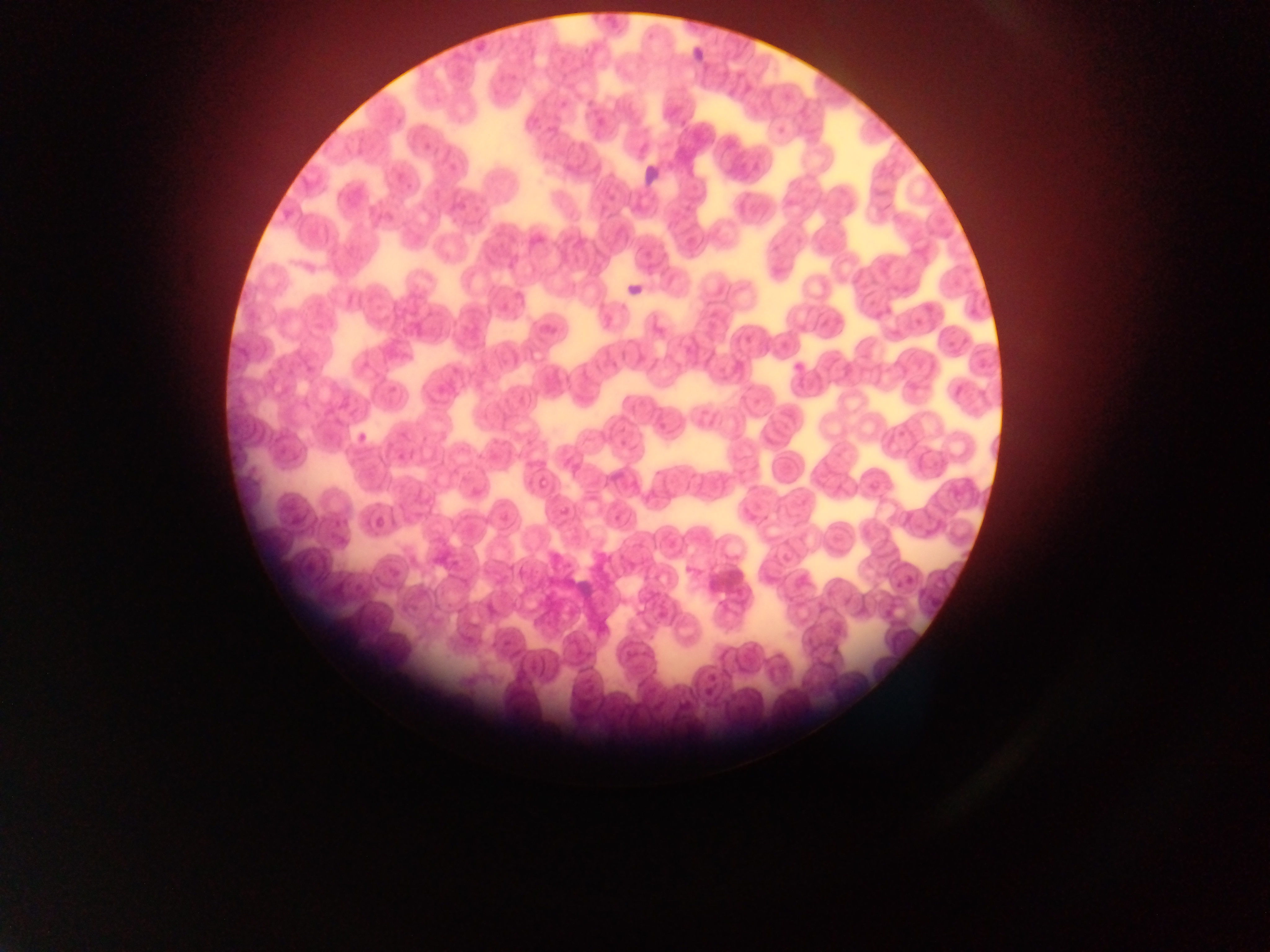 Approximate bounding boxes as (left, top, right, bottom) in pixels. Malaria parasite locations: (527, 349, 547, 361), (534, 473, 550, 486), (372, 510, 390, 527), (634, 600, 646, 613). Photographed through a microscope with a mobile-phone camera. Collected in Ghana. One field of view. Thin blood smear. Image is 1270×952 pixels.